Identify the parasite.
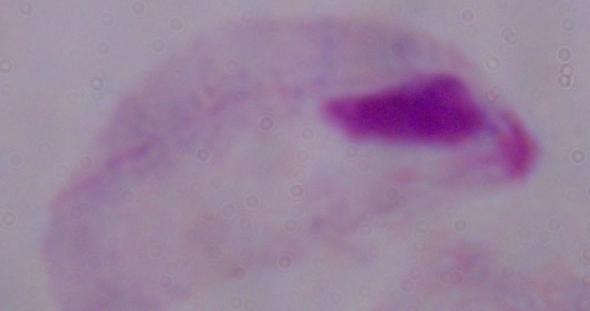
A trichomonad.

Micrograph. 1000x magnification.